Report the malaria status.
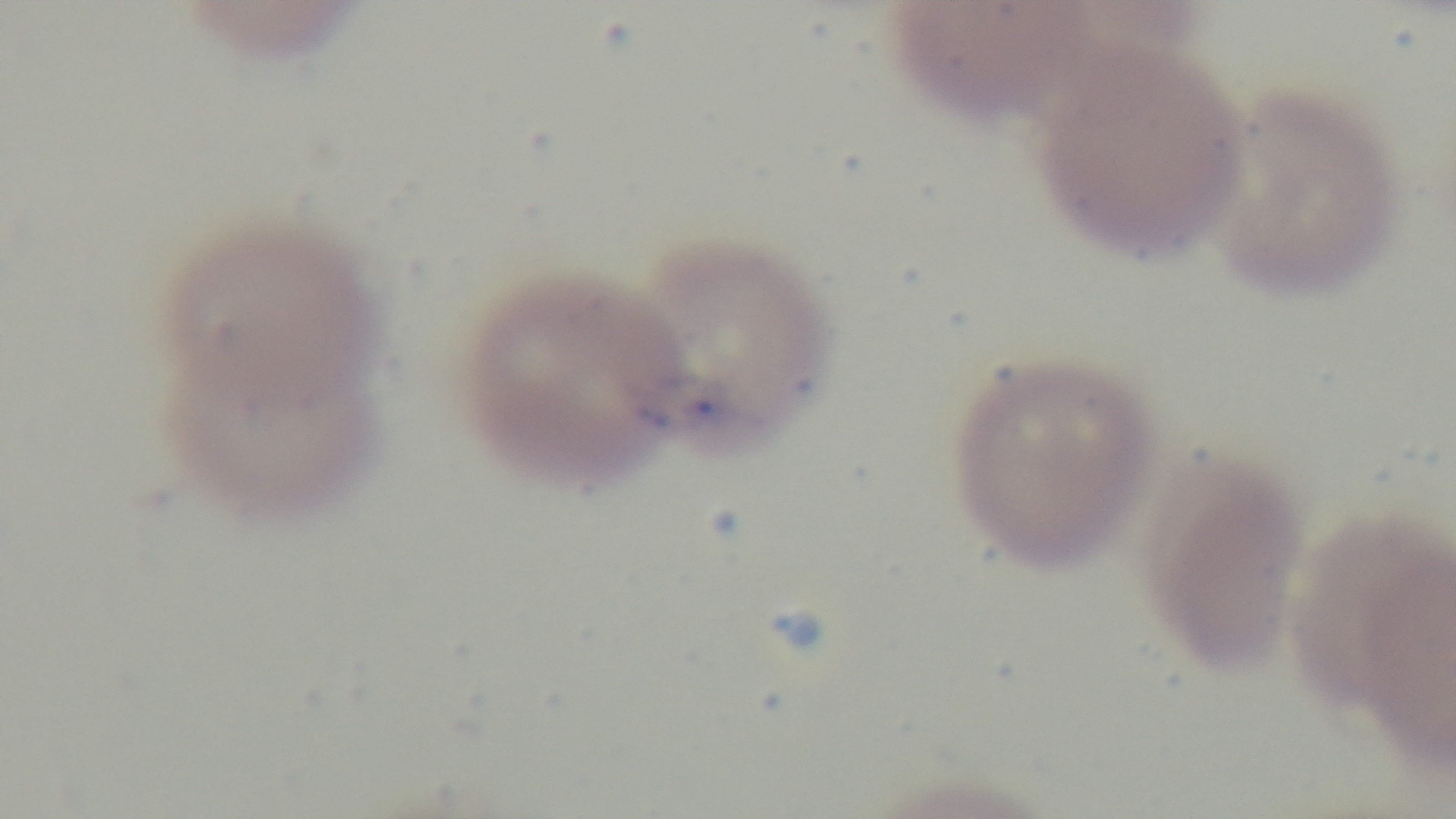

Infected.

Captured with a mounted 4K digital camera. 100x oil-immersion objective. Light microscopy. One field from the slide. Preparation: thin smear. Giemsa stain.